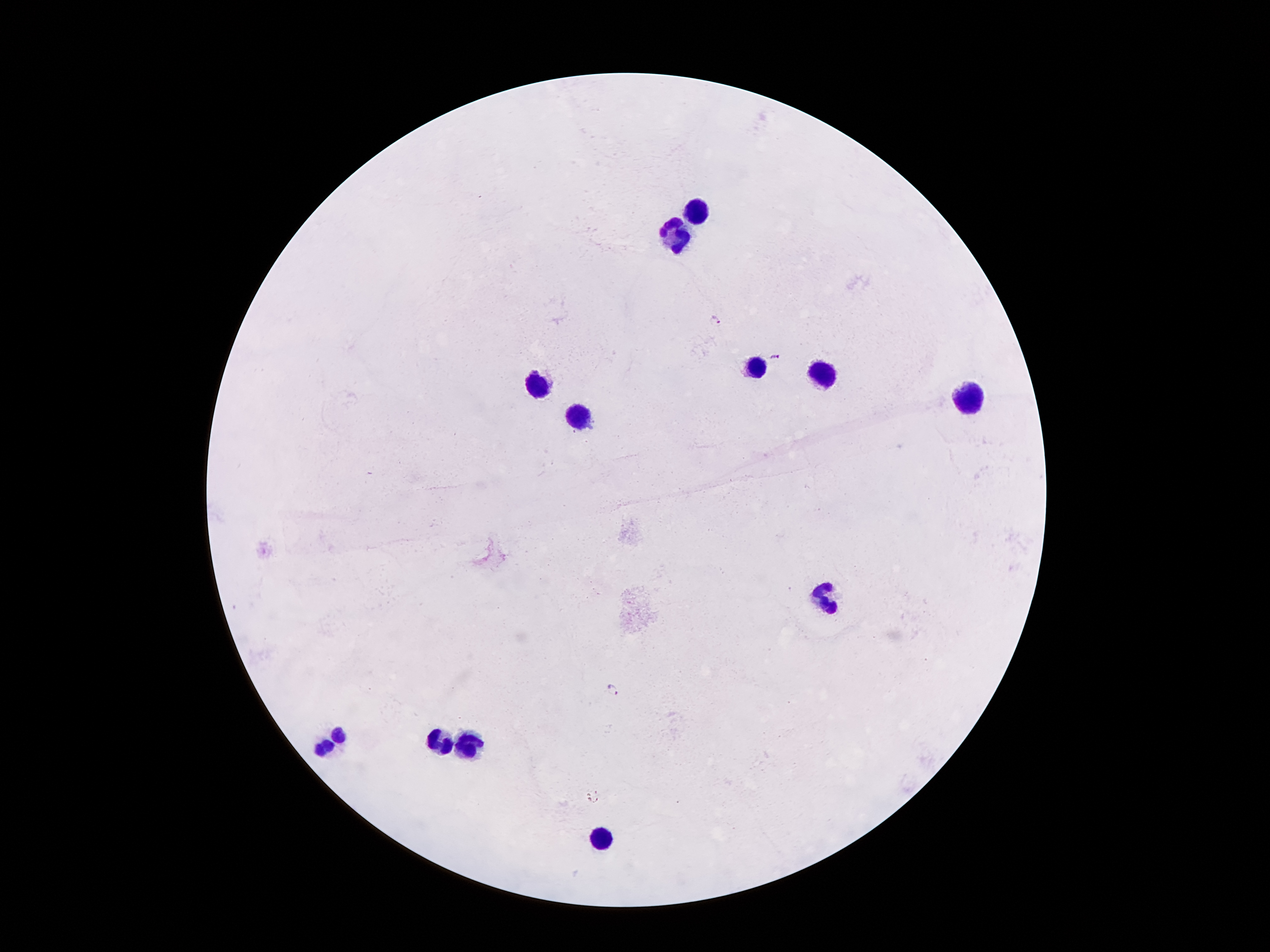
Approximate centers as {x, y} in pixels. Malaria parasite locations: {715, 320}, {775, 358}, {612, 691}. Leukocyte locations: {691, 210}, {674, 235}, {755, 367}, {820, 372}, {540, 383}, {971, 398}, {579, 414}, {825, 596}, {341, 735}, {470, 742}, {450, 747}, {323, 749}, {598, 840}. Giemsa-stained preparation. One field from this slide. Patient malaria status: positive for Plasmodium falciparum. Photographed through the microscope eyepiece with a smartphone camera. Thick peripheral-blood smear. Image is 1270×952 pixels. 100x magnification.